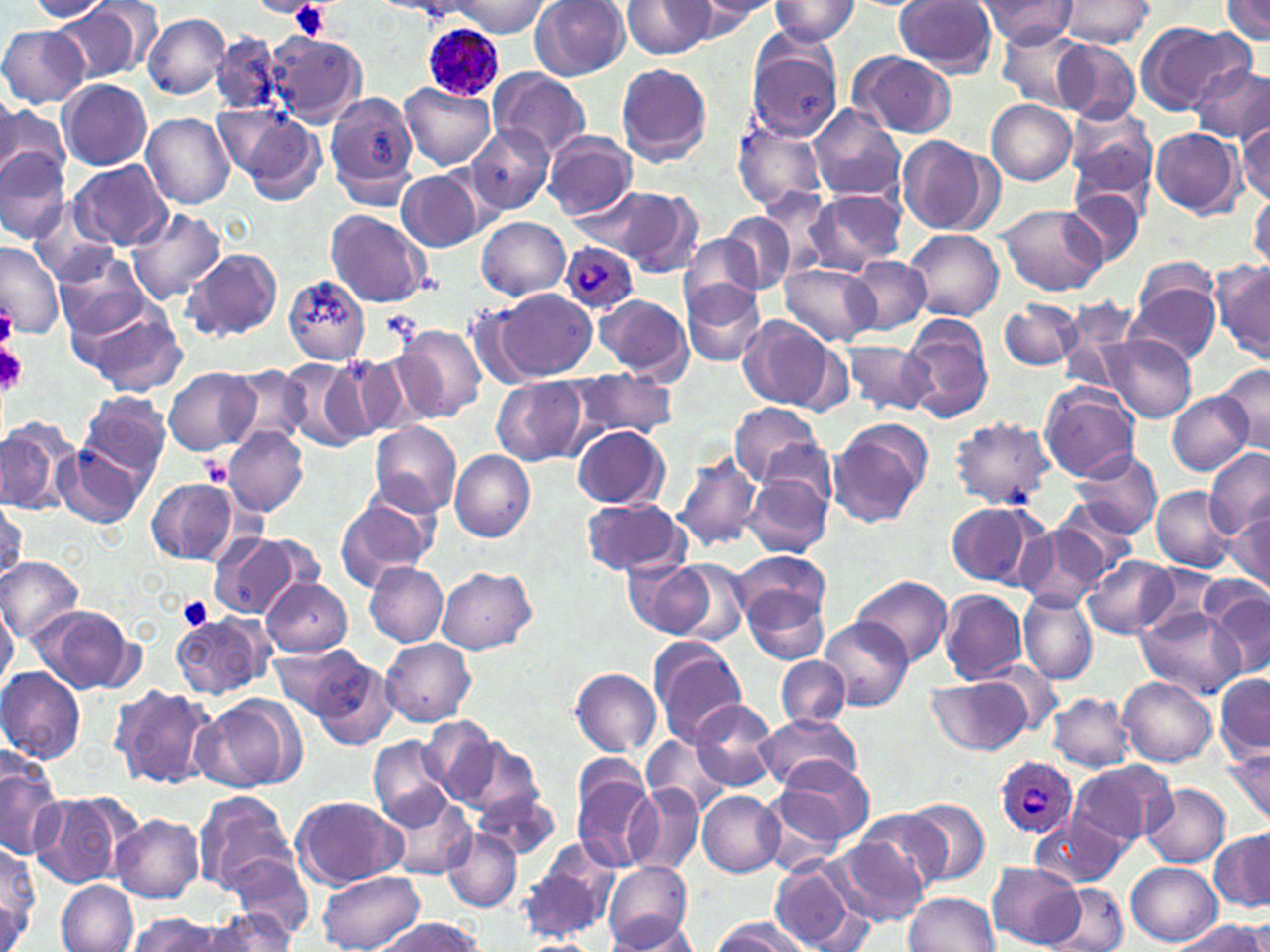

Plasmodium ovale-infected red blood cell locations = approximate bounding boxes as named x1/y1/x2/y2 corners in pixels: (x1=422, y1=23, x2=504, y2=103), (x1=560, y1=245, x2=638, y2=315), (x1=995, y1=756, x2=1078, y2=840)
slide-level diagnosis = Plasmodium ovale
magnification = 1000x
stain = May-Grünwald-Giemsa
platelet locations = approximate bounding boxes as named x1/y1/x2/y2 corners in pixels: (x1=258, y1=0, x2=319, y2=20), (x1=288, y1=2, x2=331, y2=40), (x1=0, y1=304, x2=15, y2=347), (x1=0, y1=344, x2=27, y2=395), (x1=178, y1=596, x2=214, y2=631)
preparation = thin blood smear
uninfected red blood cell locations = approximate bounding boxes as named x1/y1/x2/y2 corners in pixels: (x1=29, y1=0, x2=114, y2=22), (x1=691, y1=0, x2=782, y2=22), (x1=976, y1=0, x2=1078, y2=46), (x1=1057, y1=0, x2=1154, y2=50), (x1=250, y1=1, x2=318, y2=17), (x1=449, y1=1, x2=549, y2=36), (x1=531, y1=1, x2=630, y2=82), (x1=624, y1=1, x2=716, y2=57), (x1=677, y1=1, x2=771, y2=42), (x1=769, y1=1, x2=859, y2=46), (x1=895, y1=1, x2=999, y2=76), (x1=1223, y1=1, x2=1270, y2=43), (x1=54, y1=3, x2=150, y2=82), (x1=142, y1=13, x2=230, y2=98), (x1=1135, y1=22, x2=1244, y2=115), (x1=0, y1=24, x2=89, y2=107), (x1=998, y1=25, x2=1091, y2=107), (x1=210, y1=31, x2=284, y2=115), (x1=266, y1=32, x2=367, y2=126), (x1=1054, y1=39, x2=1142, y2=122), (x1=747, y1=41, x2=844, y2=144), (x1=848, y1=52, x2=957, y2=139), (x1=616, y1=62, x2=713, y2=167), (x1=1190, y1=63, x2=1270, y2=144), (x1=488, y1=68, x2=591, y2=158), (x1=59, y1=79, x2=152, y2=170), (x1=399, y1=84, x2=496, y2=169), (x1=326, y1=90, x2=418, y2=203), (x1=0, y1=95, x2=23, y2=176), (x1=0, y1=100, x2=68, y2=192), (x1=986, y1=100, x2=1076, y2=184), (x1=1065, y1=103, x2=1159, y2=203), (x1=807, y1=104, x2=907, y2=203), (x1=226, y1=106, x2=327, y2=204), (x1=142, y1=112, x2=236, y2=209), (x1=1237, y1=119, x2=1270, y2=206), (x1=468, y1=123, x2=554, y2=214), (x1=732, y1=123, x2=829, y2=213), (x1=1150, y1=127, x2=1243, y2=217), (x1=542, y1=132, x2=636, y2=220), (x1=896, y1=134, x2=999, y2=235), (x1=0, y1=147, x2=71, y2=244), (x1=69, y1=159, x2=171, y2=251), (x1=397, y1=170, x2=484, y2=253), (x1=755, y1=184, x2=843, y2=280), (x1=604, y1=187, x2=703, y2=275), (x1=1063, y1=187, x2=1144, y2=270), (x1=571, y1=188, x2=672, y2=257), (x1=802, y1=188, x2=907, y2=274), (x1=1248, y1=194, x2=1269, y2=271), (x1=28, y1=200, x2=116, y2=286), (x1=998, y1=204, x2=1109, y2=295), (x1=127, y1=208, x2=225, y2=305), (x1=326, y1=209, x2=431, y2=308), (x1=720, y1=213, x2=795, y2=293), (x1=477, y1=217, x2=569, y2=299), (x1=904, y1=229, x2=1004, y2=322), (x1=680, y1=233, x2=764, y2=315), (x1=0, y1=240, x2=63, y2=339), (x1=183, y1=247, x2=282, y2=341), (x1=55, y1=254, x2=153, y2=342), (x1=846, y1=256, x2=930, y2=335), (x1=1212, y1=258, x2=1270, y2=363), (x1=782, y1=262, x2=879, y2=346), (x1=282, y1=274, x2=370, y2=363), (x1=1129, y1=276, x2=1220, y2=366), (x1=682, y1=279, x2=767, y2=367), (x1=500, y1=290, x2=595, y2=380), (x1=595, y1=294, x2=692, y2=381), (x1=999, y1=298, x2=1086, y2=371), (x1=83, y1=303, x2=186, y2=398), (x1=465, y1=305, x2=540, y2=390), (x1=898, y1=314, x2=993, y2=422), (x1=738, y1=316, x2=849, y2=414), (x1=397, y1=324, x2=486, y2=420), (x1=1101, y1=334, x2=1197, y2=421), (x1=842, y1=341, x2=933, y2=417), (x1=350, y1=351, x2=437, y2=438), (x1=321, y1=354, x2=402, y2=445), (x1=286, y1=356, x2=376, y2=451), (x1=1215, y1=364, x2=1270, y2=454), (x1=224, y1=367, x2=308, y2=449), (x1=165, y1=368, x2=259, y2=456), (x1=570, y1=369, x2=675, y2=442), (x1=492, y1=377, x2=587, y2=465), (x1=1038, y1=382, x2=1140, y2=481), (x1=79, y1=391, x2=172, y2=481), (x1=1166, y1=392, x2=1254, y2=474), (x1=729, y1=403, x2=826, y2=489), (x1=0, y1=416, x2=76, y2=516), (x1=951, y1=416, x2=1055, y2=509), (x1=827, y1=419, x2=932, y2=528), (x1=369, y1=420, x2=462, y2=516), (x1=571, y1=424, x2=669, y2=509), (x1=223, y1=427, x2=308, y2=516), (x1=56, y1=441, x2=152, y2=528), (x1=1070, y1=447, x2=1163, y2=538), (x1=1205, y1=449, x2=1270, y2=538), (x1=451, y1=450, x2=536, y2=542), (x1=673, y1=452, x2=760, y2=552), (x1=743, y1=470, x2=833, y2=560), (x1=147, y1=479, x2=237, y2=564), (x1=1149, y1=486, x2=1237, y2=570), (x1=334, y1=490, x2=437, y2=590), (x1=579, y1=497, x2=689, y2=577), (x1=0, y1=498, x2=25, y2=583), (x1=1054, y1=498, x2=1145, y2=580), (x1=944, y1=500, x2=1048, y2=590), (x1=1229, y1=505, x2=1270, y2=591), (x1=1017, y1=527, x2=1108, y2=611), (x1=209, y1=533, x2=315, y2=619), (x1=733, y1=551, x2=829, y2=630), (x1=1083, y1=555, x2=1179, y2=639), (x1=0, y1=557, x2=84, y2=641), (x1=624, y1=559, x2=715, y2=641), (x1=665, y1=560, x2=753, y2=646), (x1=364, y1=563, x2=448, y2=647), (x1=437, y1=566, x2=537, y2=653), (x1=1137, y1=568, x2=1226, y2=640), (x1=854, y1=573, x2=952, y2=667), (x1=261, y1=576, x2=352, y2=657), (x1=1200, y1=587, x2=1270, y2=673), (x1=746, y1=588, x2=830, y2=663), (x1=938, y1=588, x2=1027, y2=684), (x1=1018, y1=591, x2=1098, y2=687), (x1=0, y1=600, x2=19, y2=693), (x1=32, y1=605, x2=137, y2=694), (x1=1135, y1=607, x2=1244, y2=699), (x1=171, y1=615, x2=271, y2=699), (x1=819, y1=618, x2=914, y2=712), (x1=646, y1=636, x2=747, y2=747), (x1=381, y1=639, x2=476, y2=726), (x1=272, y1=646, x2=361, y2=718), (x1=308, y1=654, x2=398, y2=752), (x1=776, y1=656, x2=849, y2=728), (x1=0, y1=666, x2=86, y2=764), (x1=569, y1=667, x2=661, y2=755), (x1=1214, y1=674, x2=1270, y2=761), (x1=1119, y1=676, x2=1217, y2=766), (x1=924, y1=679, x2=1033, y2=756), (x1=110, y1=684, x2=218, y2=790), (x1=1049, y1=692, x2=1134, y2=771), (x1=195, y1=694, x2=306, y2=793), (x1=690, y1=698, x2=781, y2=794), (x1=756, y1=713, x2=863, y2=791), (x1=417, y1=717, x2=501, y2=804), (x1=445, y1=734, x2=543, y2=819), (x1=642, y1=735, x2=729, y2=817), (x1=369, y1=736, x2=455, y2=828), (x1=1222, y1=748, x2=1270, y2=826), (x1=0, y1=752, x2=63, y2=859), (x1=769, y1=757, x2=876, y2=849), (x1=1069, y1=760, x2=1174, y2=850), (x1=570, y1=769, x2=658, y2=874), (x1=755, y1=780, x2=855, y2=877), (x1=626, y1=783, x2=702, y2=874), (x1=1141, y1=783, x2=1230, y2=867), (x1=472, y1=789, x2=561, y2=862), (x1=380, y1=790, x2=478, y2=881), (x1=29, y1=791, x2=133, y2=889), (x1=193, y1=791, x2=296, y2=892), (x1=698, y1=791, x2=784, y2=876), (x1=293, y1=795, x2=405, y2=887), (x1=903, y1=798, x2=990, y2=886), (x1=852, y1=808, x2=949, y2=895), (x1=111, y1=814, x2=205, y2=902), (x1=1033, y1=814, x2=1128, y2=888), (x1=442, y1=827, x2=522, y2=912), (x1=1212, y1=830, x2=1270, y2=913), (x1=828, y1=836, x2=931, y2=925), (x1=1, y1=839, x2=40, y2=948), (x1=224, y1=850, x2=314, y2=942), (x1=516, y1=850, x2=615, y2=945), (x1=601, y1=861, x2=692, y2=949), (x1=1127, y1=862, x2=1223, y2=945), (x1=768, y1=863, x2=868, y2=951), (x1=988, y1=863, x2=1085, y2=948), (x1=319, y1=870, x2=423, y2=952), (x1=57, y1=878, x2=140, y2=952), (x1=1050, y1=883, x2=1129, y2=952), (x1=903, y1=892, x2=1000, y2=952), (x1=199, y1=910, x2=297, y2=950), (x1=127, y1=913, x2=232, y2=951), (x1=606, y1=915, x2=700, y2=950), (x1=372, y1=917, x2=485, y2=952), (x1=711, y1=917, x2=810, y2=952), (x1=1177, y1=917, x2=1265, y2=952)
modality = light microscopy
field of view = one of a larger specimen
image size = 1270×952 pixels